Describe the morphology of the erythrocytes.
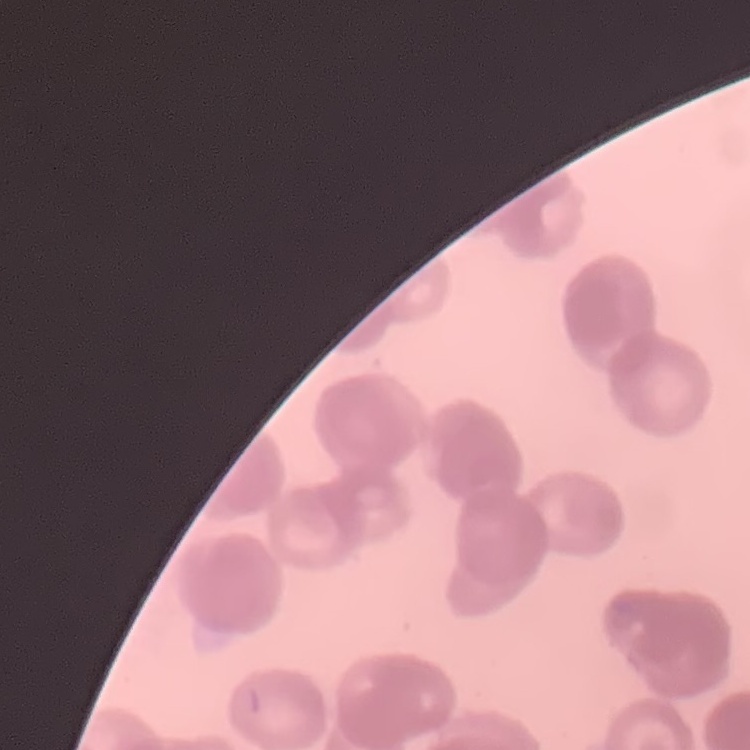

They show rouleaux formation.

Thin blood smear. One tile cut from a larger photomicrograph. Field's or Giemsa stain.